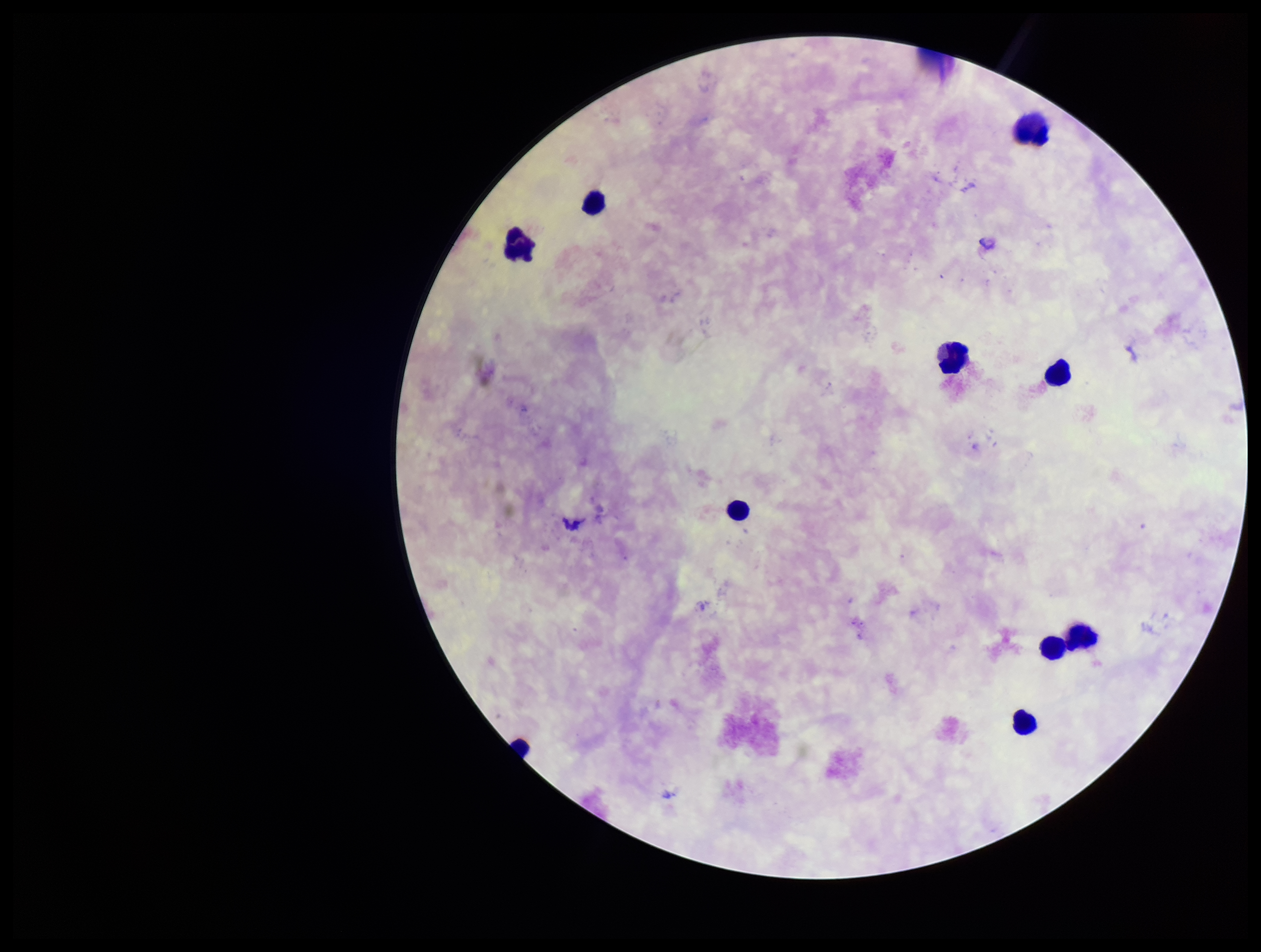 Patient malaria status: negative. Giemsa stain. Parasite count: 0. Image is 1261×952 pixels. Smartphone photograph taken through the eyepiece of a microscope. Preparation: thick. Leukocyte count: 10. Single field of view. Plasmodium parasites: none detected.